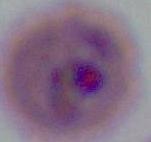 Photomicrograph. 400x or 1000x magnification. A Plasmodium parasite is shown.